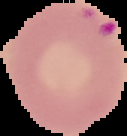
Cell region segmented out of the field of view; the surrounding area is masked to black. From a thin blood film. Image is 127×136 pixels. Result: Plasmodium parasites detected.